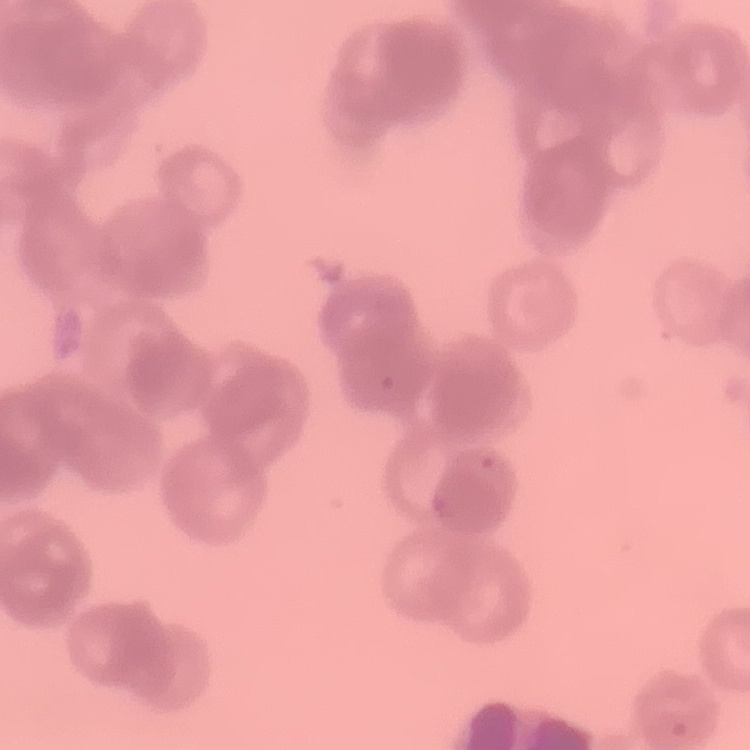

Summary:
  - Red blood cell morphology: rouleaux formation
  - Image type: square crop of a larger photomicrograph
  - Preparation: thin peripheral smear
  - Stain: Field's or Giemsa